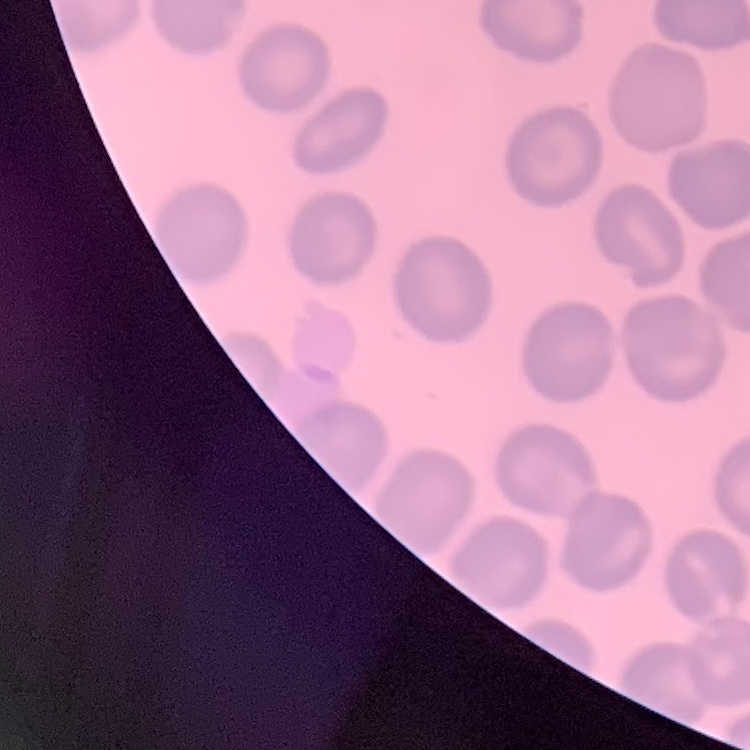
red_blood_cell_morphology: no rouleaux formation
preparation: thin peripheral smear
image_type: square crop of a larger photomicrograph
stain: Field's or Giemsa